Evaluate for Plasmodium parasites.
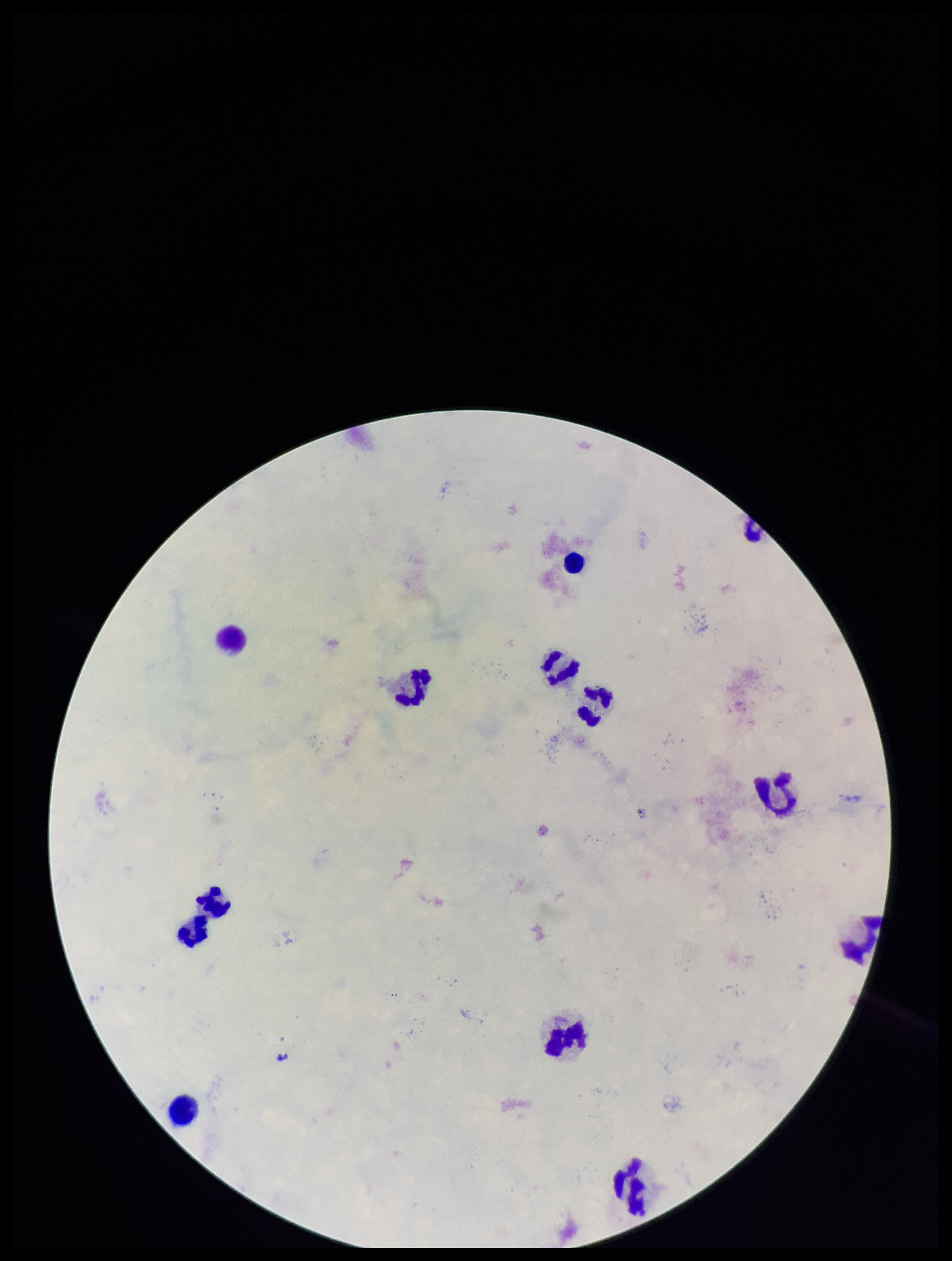
None seen.

Summary:
  - Preparation: thick blood smear
  - Stain: Giemsa
  - Patient malaria status: negative
  - Capture: smartphone photograph through the microscope eyepiece
  - Image size: 952×1261 pixels
  - Field of view: one from this slide
  - Leukocyte count: 13
  - Parasite count: 0